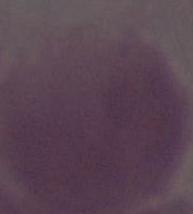

An erythrocyte is shown. Photomicrograph. Captured at 1000x magnification.